Outline every malaria parasite.
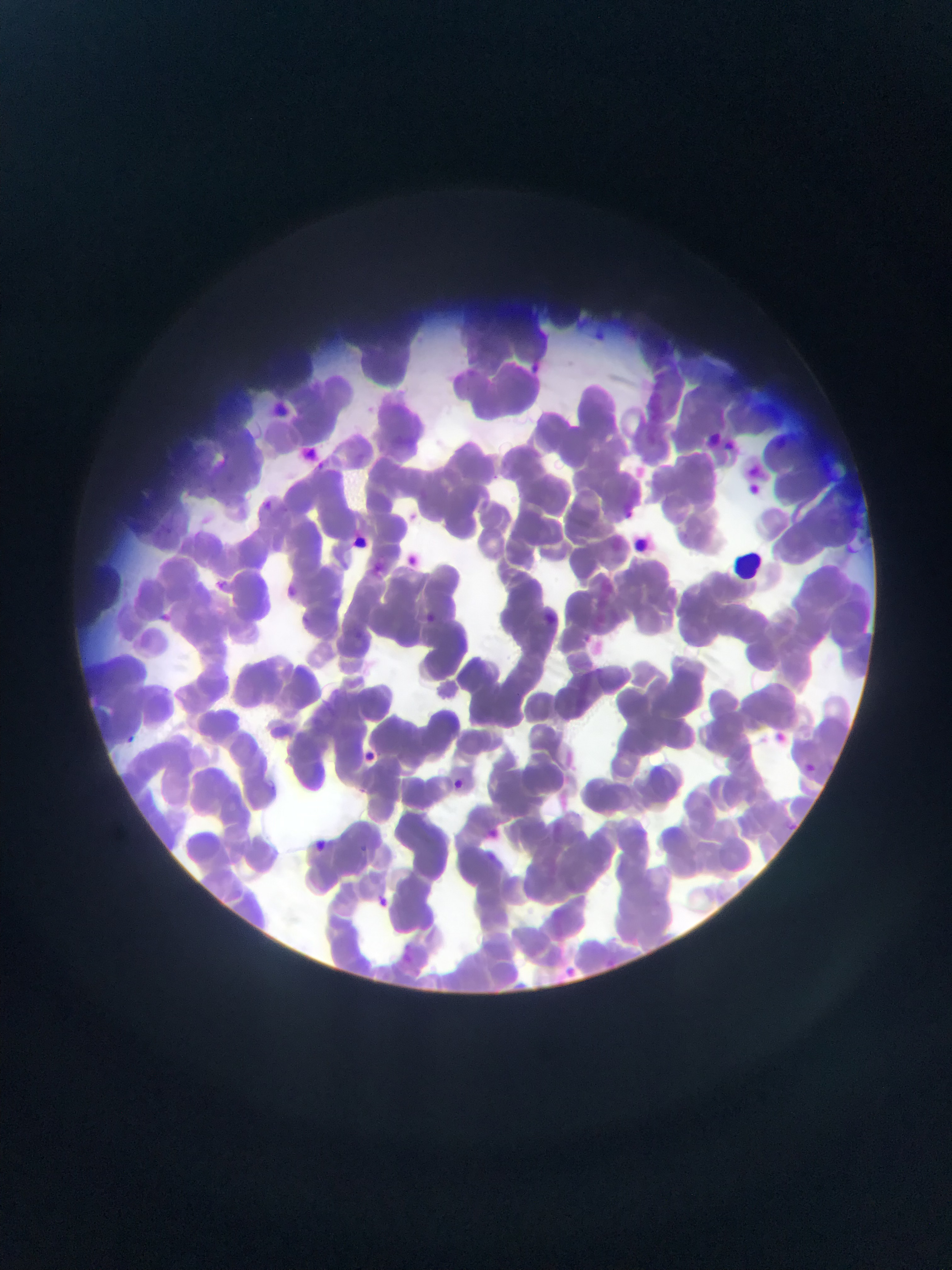

Approximate bounding boxes as (left, top, right, bottom) in pixels.
Malaria parasites: (591, 327, 619, 356), (525, 352, 547, 380), (744, 473, 768, 504), (254, 496, 278, 518), (624, 503, 640, 524), (356, 534, 377, 555), (405, 547, 420, 571), (206, 576, 232, 597), (417, 605, 440, 621), (775, 727, 796, 762), (121, 729, 141, 747), (364, 750, 388, 768), (800, 760, 819, 778), (449, 777, 467, 793), (482, 824, 505, 844), (307, 836, 330, 856), (371, 894, 392, 913).

Summary:
  - Capture: mobile-phone photograph through a microscope
  - Country: Ghana
  - Preparation: thin blood film
  - Image size: 952×1270 pixels
  - Field of view: single